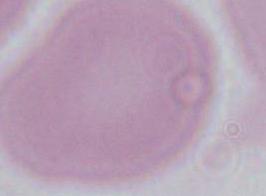
modality: micrograph
identification: erythrocyte
magnification: 1000x